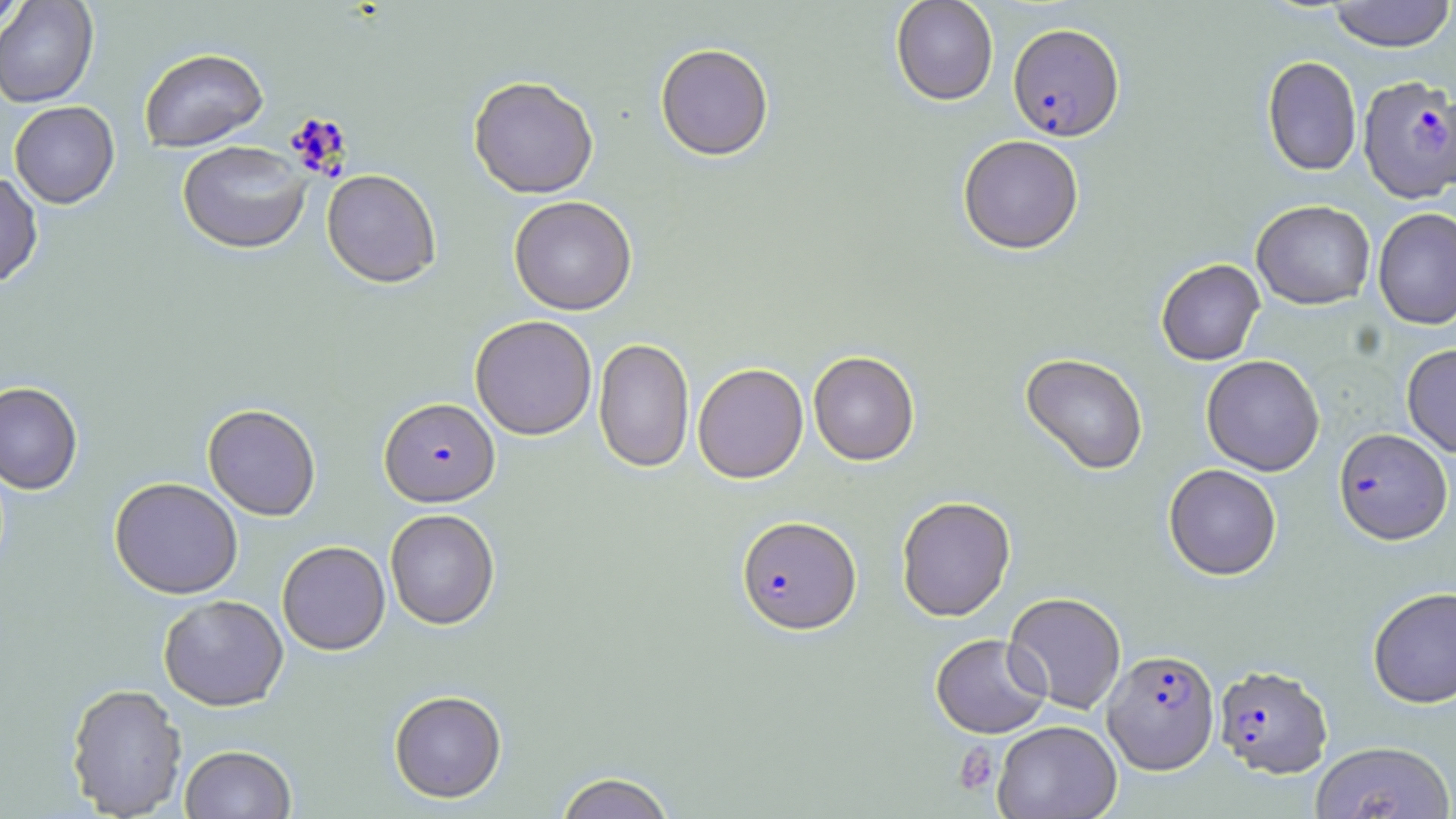
Summary:
  - Coordinate format: approximate bounding boxes as (x1, y1, x2, y2) in pixels
  - Uninfected red blood cell locations: (890, 0, 998, 105), (1327, 0, 1456, 52), (0, 1, 28, 34), (0, 1, 98, 108), (655, 43, 774, 161), (138, 48, 268, 152), (1261, 55, 1362, 177), (468, 75, 599, 198), (9, 101, 120, 208), (957, 134, 1084, 254), (177, 140, 312, 253), (322, 169, 441, 287), (0, 171, 43, 288), (509, 195, 638, 315), (1252, 199, 1375, 309), (1373, 207, 1456, 331), (1155, 259, 1265, 365), (470, 315, 598, 440), (593, 337, 694, 473), (1402, 343, 1456, 457), (808, 351, 920, 466), (1020, 353, 1148, 476), (1201, 354, 1325, 476), (693, 362, 809, 483), (0, 381, 83, 494), (202, 403, 321, 520), (1163, 463, 1282, 580), (109, 477, 243, 599), (896, 496, 1016, 621), (384, 508, 500, 629), (277, 540, 390, 655), (1368, 586, 1456, 708), (158, 594, 288, 710), (1005, 594, 1129, 717), (930, 633, 1050, 738), (66, 683, 187, 817), (389, 689, 506, 803), (993, 720, 1122, 819), (1310, 740, 1455, 819), (179, 744, 296, 818), (554, 771, 677, 819)
  - Plasmodium falciparum-infected red blood cell locations: (1008, 22, 1125, 141), (1358, 76, 1456, 202), (380, 397, 500, 506), (1334, 427, 1452, 544), (736, 515, 861, 635), (1102, 648, 1219, 774), (1213, 664, 1333, 777)
  - Platelet locations: (953, 742, 998, 795)
  - Slide-level diagnosis: Plasmodium falciparum
  - Modality: optical microscopy
  - Magnification: 1000x
  - Preparation: thin blood film
  - Stain: May-Grünwald-Giemsa
  - Field of view: single
  - Image size: 1456×819 pixels